Assess this cell for malaria.
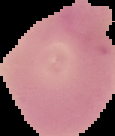

Uninfected.

Image is 115×136 pixels. Cell region segmented out of the field of view; the surrounding area is masked to black. From a thin blood film.